Report the malaria status of this cell.
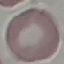
Uninfected.

Summary:
  - Preparation: thin smear
  - Capture: smartphone camera at the microscope eyepiece
  - Stain: Giemsa
  - Image type: automatically extracted cell patch, resized to 64 × 64 pixels